Assess this cell for malaria.
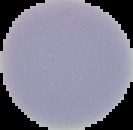
It is uninfected.

Summary:
  - Image type: segmented cell region with the area outside set to black
  - Image size: 133×130 pixels
  - Preparation: thin blood smear